State which parasite is depicted.
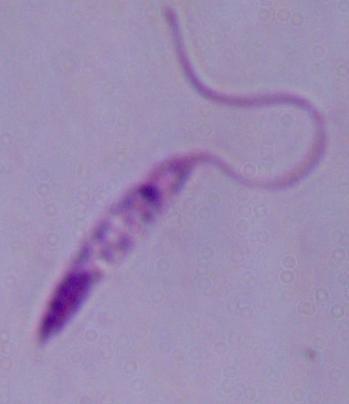

This is Leishmania.

1000x magnification. Photomicrograph.